Name the blood parasite species.
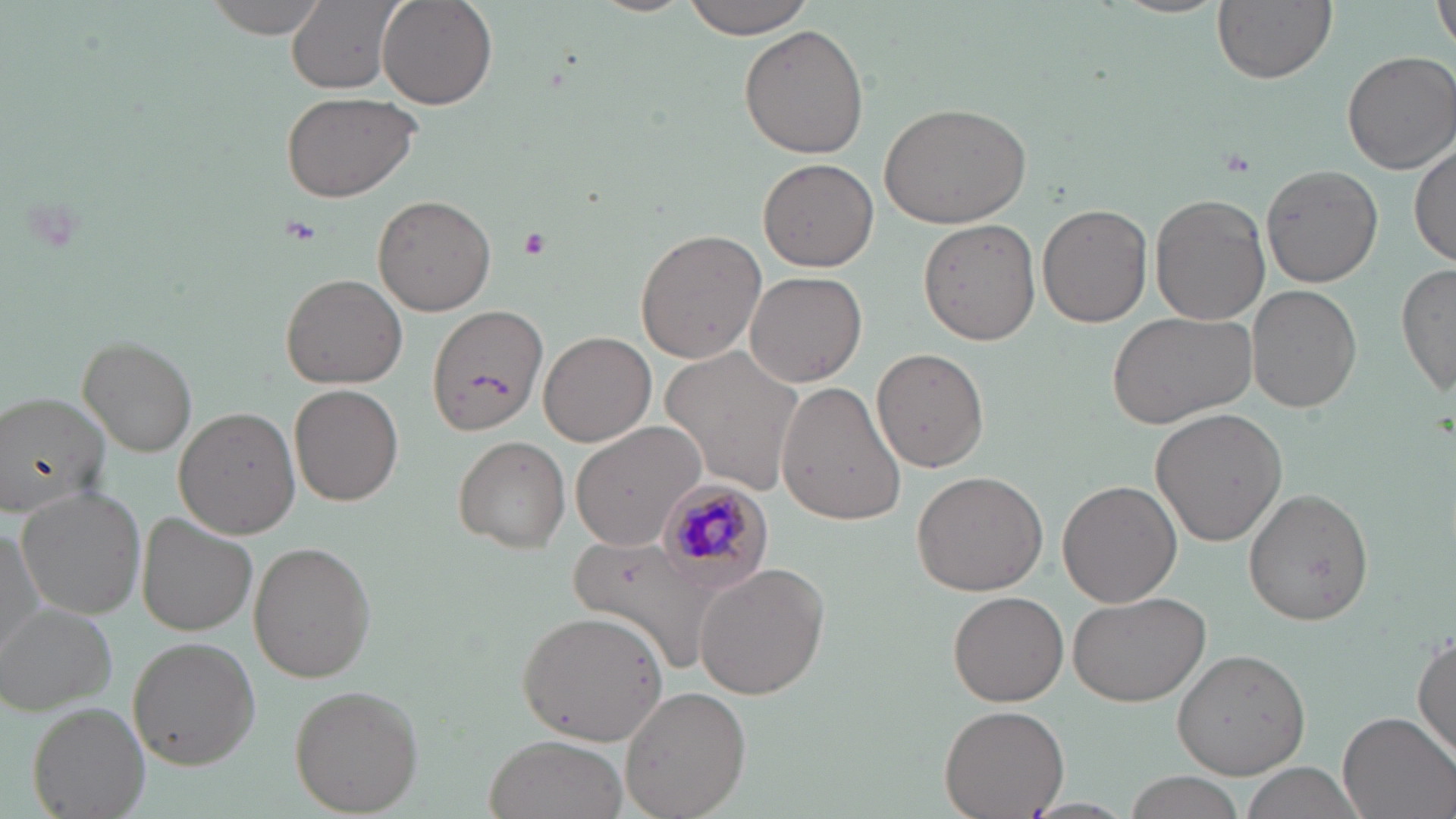

Plasmodium malariae.

Summary:
  - Coordinate format: approximate bounding boxes as [x1, y1, x2, y2] in pixels
  - Plasmodium malariae-infected red blood cell locations: [656, 478, 773, 583]
  - Uninfected red blood cell locations: [202, 0, 332, 38], [286, 0, 400, 93], [377, 0, 497, 110], [679, 0, 818, 38], [1213, 0, 1335, 83], [1434, 0, 1456, 60], [739, 24, 869, 158], [1340, 50, 1454, 175], [280, 90, 420, 202], [879, 101, 1031, 229], [1411, 140, 1455, 269], [758, 158, 878, 273], [1260, 165, 1384, 286], [1149, 193, 1271, 325], [373, 195, 496, 315], [1038, 202, 1152, 327], [919, 218, 1041, 345], [634, 229, 767, 363], [1396, 263, 1455, 399], [745, 270, 868, 387], [281, 273, 408, 389], [1246, 285, 1361, 413], [425, 305, 548, 437], [1106, 310, 1259, 429], [538, 330, 656, 446], [78, 337, 195, 457], [874, 348, 988, 471], [665, 349, 807, 495], [776, 382, 907, 525], [290, 384, 403, 506], [1, 393, 114, 515], [174, 405, 301, 540], [1149, 407, 1287, 547], [569, 422, 706, 552], [452, 435, 571, 552], [910, 469, 1048, 595], [1058, 480, 1181, 607], [16, 487, 147, 619], [1242, 488, 1374, 626], [136, 512, 256, 636], [0, 518, 47, 664], [249, 540, 377, 685], [693, 563, 829, 699], [1067, 590, 1210, 709], [950, 591, 1070, 707], [3, 604, 118, 714], [516, 610, 669, 745], [1412, 629, 1456, 764], [127, 637, 260, 769], [1171, 646, 1312, 777], [290, 683, 421, 814], [620, 684, 750, 819], [28, 701, 151, 819], [940, 704, 1068, 817], [1338, 709, 1454, 819], [485, 734, 626, 818], [1235, 761, 1362, 819], [1122, 771, 1248, 819]
  - Platelet locations: [515, 225, 551, 258]
  - Stain: May-Grünwald-Giemsa
  - Field of view: single
  - Preparation: thin blood film
  - Modality: light microscopy
  - Image size: 1456×819 pixels
  - Magnification: 1000x